Report the malaria status of this cell.
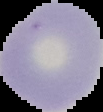
It is uninfected.

{
  "preparation": "thin blood smear",
  "image_type": "segmented cell region on a black background",
  "image_size": "103×112 pixels"
}